Outline each Plasmodium ovale-infected red blood cell.
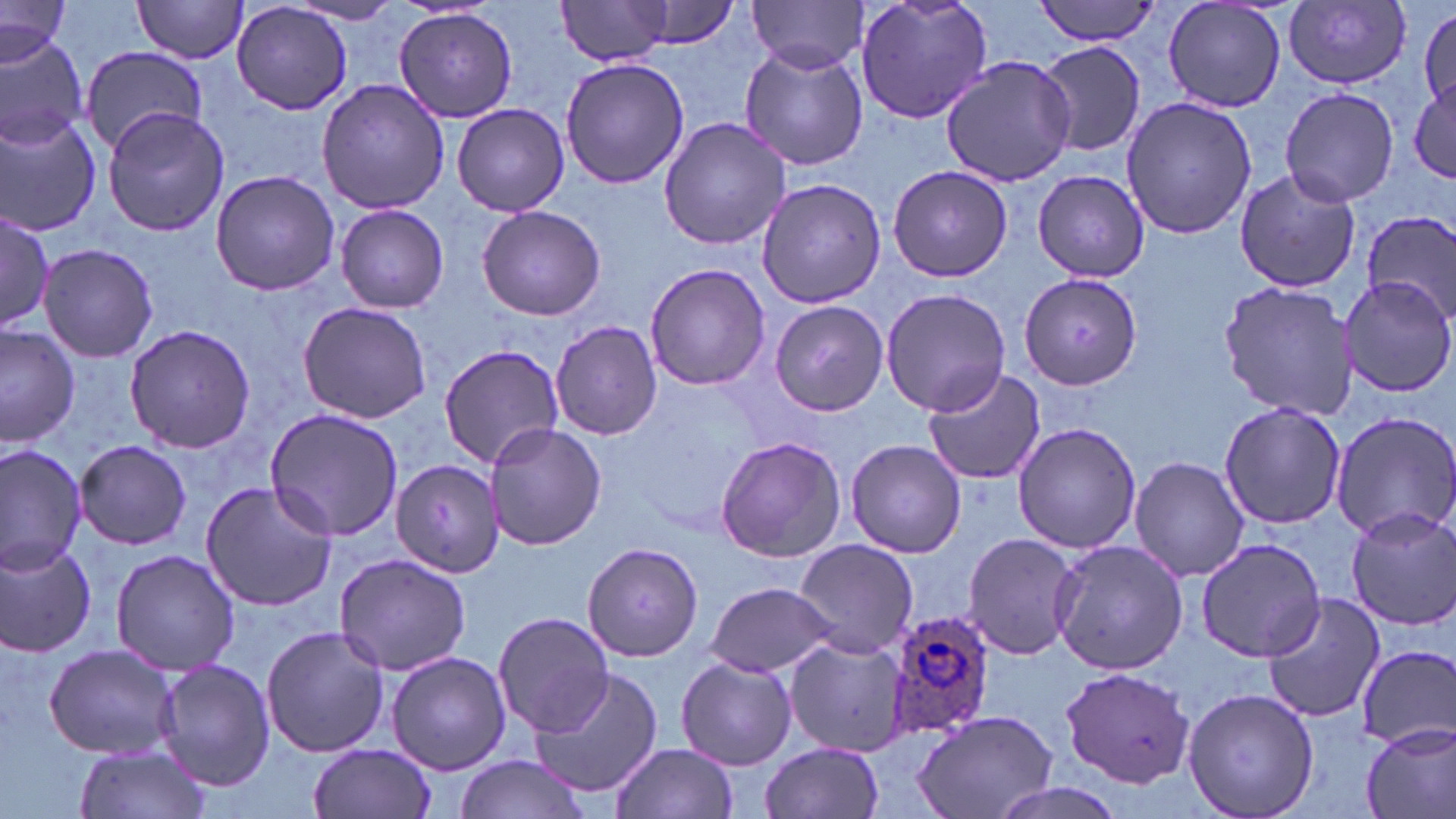
Approximate bounding boxes as named x1/y1/x2/y2 corners in pixels.
Plasmodium ovale-infected red blood cells: (x1=883, y1=607, x2=1002, y2=745).

Summary:
  - Uninfected red blood cell locations: (x1=131, y1=0, x2=250, y2=62), (x1=556, y1=0, x2=677, y2=66), (x1=748, y1=0, x2=869, y2=72), (x1=853, y1=0, x2=994, y2=126), (x1=1033, y1=0, x2=1164, y2=46), (x1=1159, y1=0, x2=1289, y2=113), (x1=631, y1=1, x2=740, y2=49), (x1=1282, y1=1, x2=1411, y2=86), (x1=231, y1=2, x2=353, y2=116), (x1=290, y1=2, x2=406, y2=26), (x1=0, y1=4, x2=71, y2=64), (x1=1416, y1=7, x2=1455, y2=113), (x1=394, y1=8, x2=517, y2=124), (x1=0, y1=33, x2=89, y2=150), (x1=1036, y1=41, x2=1147, y2=157), (x1=78, y1=44, x2=209, y2=155), (x1=738, y1=45, x2=868, y2=171), (x1=939, y1=56, x2=1076, y2=188), (x1=560, y1=58, x2=689, y2=190), (x1=1409, y1=75, x2=1456, y2=189), (x1=317, y1=77, x2=450, y2=215), (x1=1279, y1=87, x2=1399, y2=207), (x1=1121, y1=97, x2=1256, y2=238), (x1=451, y1=103, x2=571, y2=217), (x1=103, y1=106, x2=229, y2=237), (x1=0, y1=115, x2=101, y2=236), (x1=657, y1=115, x2=793, y2=251), (x1=888, y1=165, x2=1013, y2=281), (x1=210, y1=169, x2=339, y2=296), (x1=1029, y1=169, x2=1149, y2=281), (x1=1233, y1=169, x2=1361, y2=294), (x1=754, y1=177, x2=889, y2=307), (x1=335, y1=203, x2=449, y2=313), (x1=476, y1=205, x2=606, y2=320), (x1=0, y1=209, x2=54, y2=334), (x1=1364, y1=213, x2=1456, y2=324), (x1=38, y1=244, x2=157, y2=362), (x1=642, y1=261, x2=769, y2=391), (x1=1017, y1=271, x2=1142, y2=391), (x1=1339, y1=275, x2=1456, y2=398), (x1=1217, y1=279, x2=1357, y2=421), (x1=881, y1=287, x2=1010, y2=416), (x1=768, y1=300, x2=888, y2=417), (x1=297, y1=301, x2=433, y2=425), (x1=550, y1=320, x2=663, y2=441), (x1=0, y1=322, x2=80, y2=447), (x1=124, y1=323, x2=259, y2=453), (x1=438, y1=344, x2=564, y2=468), (x1=921, y1=366, x2=1047, y2=487), (x1=1217, y1=401, x2=1348, y2=531), (x1=265, y1=407, x2=406, y2=542), (x1=1328, y1=409, x2=1456, y2=541), (x1=484, y1=422, x2=606, y2=554), (x1=1012, y1=422, x2=1141, y2=555), (x1=714, y1=436, x2=845, y2=563), (x1=845, y1=438, x2=966, y2=559), (x1=74, y1=440, x2=190, y2=550), (x1=0, y1=442, x2=87, y2=574), (x1=1130, y1=456, x2=1248, y2=582), (x1=391, y1=458, x2=504, y2=577), (x1=199, y1=481, x2=337, y2=611), (x1=1345, y1=505, x2=1456, y2=630), (x1=962, y1=532, x2=1080, y2=660), (x1=1050, y1=537, x2=1187, y2=675), (x1=1194, y1=537, x2=1326, y2=663), (x1=0, y1=538, x2=100, y2=659), (x1=794, y1=538, x2=918, y2=658), (x1=582, y1=541, x2=702, y2=661), (x1=110, y1=548, x2=240, y2=676), (x1=334, y1=554, x2=473, y2=677), (x1=707, y1=580, x2=839, y2=678), (x1=1262, y1=593, x2=1386, y2=724), (x1=493, y1=611, x2=616, y2=737), (x1=259, y1=625, x2=390, y2=759), (x1=786, y1=636, x2=912, y2=756), (x1=1353, y1=644, x2=1456, y2=747), (x1=43, y1=645, x2=183, y2=760), (x1=386, y1=651, x2=511, y2=774), (x1=153, y1=656, x2=275, y2=791), (x1=675, y1=656, x2=798, y2=771), (x1=1060, y1=665, x2=1194, y2=790), (x1=527, y1=667, x2=663, y2=799), (x1=1181, y1=686, x2=1319, y2=819), (x1=913, y1=709, x2=1057, y2=819), (x1=1359, y1=721, x2=1456, y2=819), (x1=610, y1=741, x2=737, y2=819), (x1=308, y1=742, x2=435, y2=818), (x1=759, y1=742, x2=884, y2=819), (x1=73, y1=743, x2=213, y2=819), (x1=454, y1=754, x2=588, y2=819), (x1=982, y1=781, x2=1135, y2=819)
  - Slide-level diagnosis: Plasmodium ovale
  - Field of view: single
  - Image size: 1456×819 pixels
  - Magnification: 1000x
  - Modality: optical microscopy
  - Preparation: thin blood film
  - Stain: May-Grünwald-Giemsa